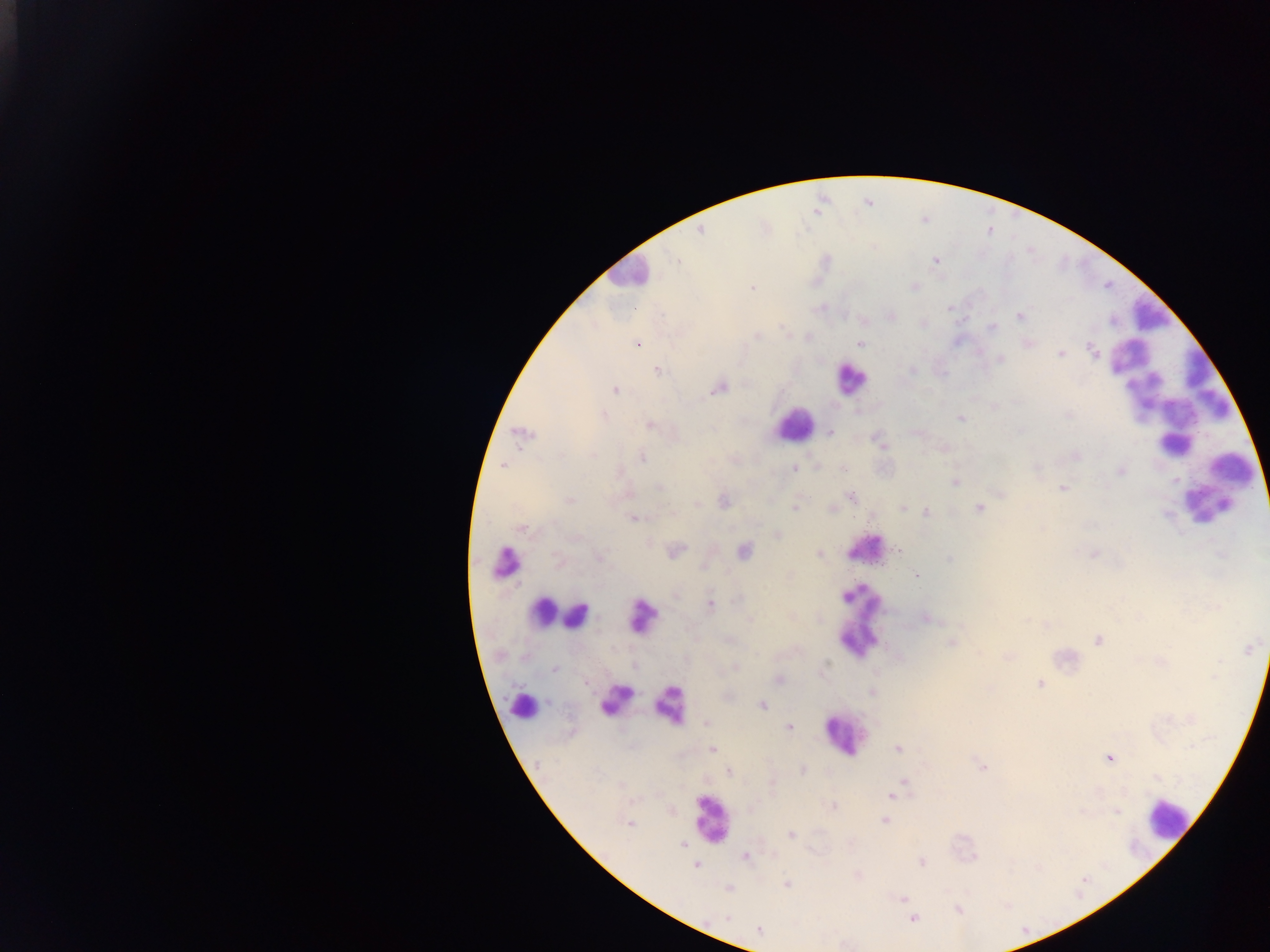

Approximate centers as (x, y) in pixels. Malaria parasite locations: (699, 231), (678, 259), (752, 289), (1019, 315), (1111, 321), (992, 328), (786, 332), (757, 337), (807, 337), (639, 344), (860, 344), (1029, 344), (1095, 352), (1059, 354), (1000, 359), (911, 370), (657, 371), (723, 388), (615, 390), (606, 416), (1069, 417), (961, 418), (648, 424), (829, 433), (942, 447), (1078, 455), (641, 456), (503, 465), (795, 468), (842, 468), (1121, 471), (955, 483), (1060, 487), (658, 490), (1001, 495), (851, 496), (568, 499), (723, 501), (694, 506), (794, 508), (979, 508), (833, 509), (902, 509), (925, 511), (1167, 514), (632, 520), (522, 528), (649, 541), (898, 551), (743, 552), (1094, 553), (819, 554), (599, 558), (949, 559), (916, 575), (736, 600), (710, 603), (926, 617), (749, 619), (1026, 620), (1045, 624), (1099, 640), (951, 643), (1248, 648), (1008, 656), (1162, 662), (829, 665), (734, 666), (1218, 666), (554, 669), (1216, 671), (1040, 684), (764, 705), (1191, 718), (706, 724), (788, 727), (712, 750), (1111, 757), (802, 770), (728, 772), (890, 797), (832, 805), (1117, 811), (884, 820), (627, 823), (790, 835), (682, 845), (744, 857), (923, 862), (694, 867), (787, 884), (727, 890), (901, 898), (958, 910), (913, 917), (726, 918), (759, 930). Thick blood film. Collected in Ghana. Image is 1270×952 pixels. Photographed through a microscope with a mobile-phone camera. Single field of view.